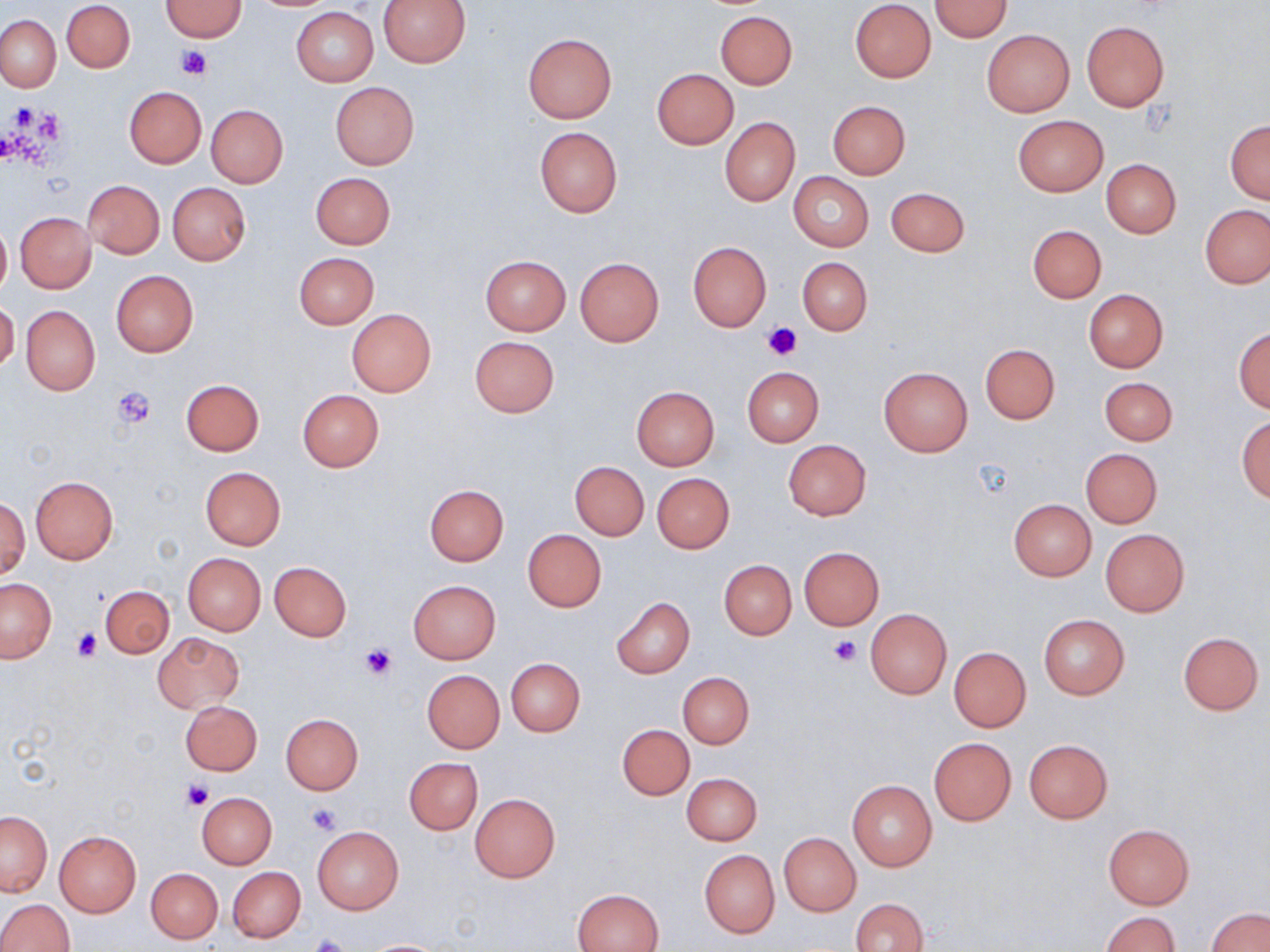
Summary:
  - Coordinate format: approximate bounding boxes as (x1,y1)-(x2,y2) corner pairs in pixels
  - Uninfected red blood cell locations: (377,0)-(471,66), (849,0)-(936,83), (62,1)-(135,73), (160,1)-(246,40), (931,1)-(1012,41), (291,7)-(378,86), (716,11)-(796,88), (0,15)-(60,91), (1082,20)-(1168,111), (981,29)-(1074,117), (523,33)-(616,122), (653,68)-(738,149), (330,82)-(419,169), (124,86)-(206,167), (828,100)-(911,179), (206,105)-(287,187), (1012,115)-(1107,196), (720,118)-(799,204), (1225,120)-(1270,204), (534,126)-(622,217), (1101,159)-(1181,239), (310,172)-(395,249), (788,172)-(873,251), (82,180)-(164,259), (167,182)-(251,264), (885,186)-(970,258), (1200,204)-(1269,289), (15,212)-(96,293), (0,223)-(10,298), (1027,224)-(1107,303), (687,242)-(772,331), (294,252)-(379,328), (480,255)-(571,334), (575,257)-(664,346), (797,257)-(872,335), (111,270)-(199,357), (1083,289)-(1169,372), (0,299)-(19,373), (20,306)-(100,394), (347,309)-(436,396), (1234,327)-(1270,413), (469,336)-(559,418), (980,344)-(1059,423), (741,366)-(823,447), (878,367)-(972,455), (1098,376)-(1178,446), (181,378)-(264,455), (631,386)-(720,471), (297,389)-(382,471), (1236,416)-(1270,502), (783,439)-(871,521), (1081,448)-(1163,528), (570,462)-(648,540), (200,467)-(286,549), (653,473)-(735,553), (30,476)-(119,563), (425,484)-(508,565), (0,497)-(29,581), (1009,499)-(1095,580), (522,529)-(607,611), (1100,529)-(1189,618), (798,546)-(884,629), (182,552)-(266,636), (719,560)-(796,639), (270,562)-(352,641), (1,578)-(56,663), (408,580)-(501,664), (101,586)-(174,658), (612,597)-(694,677), (865,609)-(951,699), (1037,614)-(1129,699), (1177,631)-(1264,714), (153,632)-(244,712), (169,635)-(252,774), (949,647)-(1030,731), (506,658)-(585,736), (423,670)-(505,753), (678,671)-(754,748), (180,700)-(263,776), (280,713)-(363,794), (618,724)-(694,799), (929,737)-(1015,825), (1024,739)-(1112,823), (404,758)-(483,834), (681,772)-(763,846), (847,780)-(936,872), (196,792)-(276,869), (469,794)-(560,883), (0,811)-(51,896), (1102,823)-(1195,910), (312,827)-(404,915), (54,831)-(141,916), (779,833)-(861,917), (699,849)-(779,937), (228,866)-(305,943), (147,868)-(222,943), (574,888)-(665,952), (850,897)-(929,952), (0,898)-(73,951), (1206,907)-(1270,952), (1102,911)-(1181,952), (360,939)-(450,951)
  - Platelet locations: (177,47)-(211,80), (764,323)-(803,360), (113,386)-(156,429), (71,629)-(101,661), (828,637)-(860,667), (359,644)-(397,680), (182,779)-(213,810), (307,804)-(341,835), (306,935)-(354,952)
  - Slide-level diagnosis: no evidence of blood parasites
  - Magnification: 1000x
  - Field of view: single
  - Modality: light microscopy
  - Preparation: thin blood film
  - Image size: 1270×952 pixels
  - Stain: May-Grünwald-Giemsa